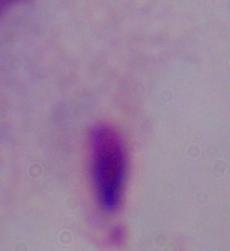

modality = micrograph
identification = trichomonad
magnification = 1000x